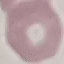

Summary:
  - Result: no malaria parasites detected
  - Stain: Giemsa
  - Image type: cell patch, automatically extracted from a larger field of view and resized to 64 × 64 pixels
  - Preparation: thin blood film
  - Capture: smartphone camera at the microscope eyepiece